Identify the blood parasite species.
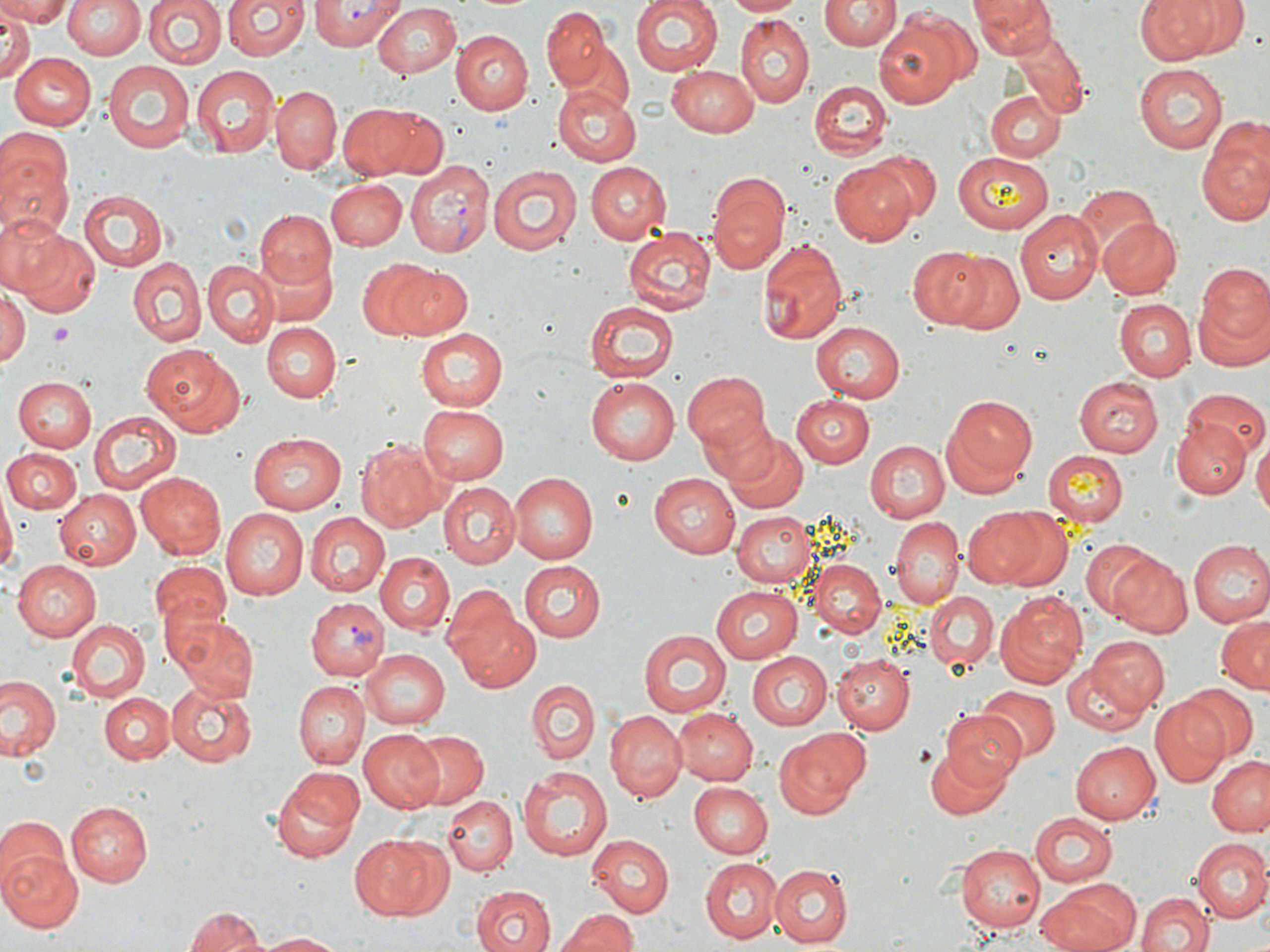
Plasmodium vivax.

Summary:
  - Coordinate format: approximate bounding boxes as named x1/y1/x2/y2 corners in pixels
  - Platelet locations: (x1=49, y1=325, x2=73, y2=345)
  - Plasmodium vivax-infected red blood cell locations: (x1=309, y1=0, x2=401, y2=50), (x1=404, y1=162, x2=493, y2=256), (x1=307, y1=599, x2=388, y2=684)
  - Uninfected red blood cell locations: (x1=1, y1=0, x2=73, y2=26), (x1=61, y1=0, x2=145, y2=60), (x1=141, y1=0, x2=225, y2=71), (x1=224, y1=0, x2=308, y2=63), (x1=629, y1=0, x2=722, y2=76), (x1=725, y1=0, x2=805, y2=17), (x1=821, y1=0, x2=897, y2=50), (x1=970, y1=0, x2=1052, y2=58), (x1=1137, y1=0, x2=1247, y2=63), (x1=369, y1=3, x2=464, y2=79), (x1=540, y1=5, x2=613, y2=92), (x1=872, y1=12, x2=971, y2=110), (x1=0, y1=14, x2=34, y2=81), (x1=734, y1=18, x2=813, y2=108), (x1=454, y1=28, x2=535, y2=113), (x1=1011, y1=31, x2=1089, y2=116), (x1=556, y1=41, x2=635, y2=115), (x1=9, y1=52, x2=96, y2=130), (x1=103, y1=60, x2=196, y2=152), (x1=1135, y1=63, x2=1227, y2=153), (x1=191, y1=65, x2=279, y2=158), (x1=666, y1=66, x2=761, y2=135), (x1=810, y1=80, x2=889, y2=160), (x1=551, y1=82, x2=643, y2=166), (x1=270, y1=85, x2=341, y2=173), (x1=985, y1=90, x2=1064, y2=163), (x1=337, y1=103, x2=420, y2=179), (x1=370, y1=107, x2=450, y2=179), (x1=1, y1=122, x2=73, y2=213), (x1=1199, y1=122, x2=1270, y2=225), (x1=869, y1=149, x2=942, y2=220), (x1=952, y1=152, x2=1053, y2=234), (x1=1, y1=160, x2=72, y2=242), (x1=584, y1=161, x2=670, y2=243), (x1=830, y1=161, x2=918, y2=244), (x1=487, y1=164, x2=581, y2=257), (x1=706, y1=173, x2=790, y2=273), (x1=327, y1=179, x2=406, y2=249), (x1=1072, y1=183, x2=1160, y2=269), (x1=79, y1=190, x2=167, y2=270), (x1=254, y1=209, x2=335, y2=291), (x1=1016, y1=210, x2=1104, y2=305), (x1=0, y1=213, x2=71, y2=293), (x1=1099, y1=217, x2=1181, y2=299), (x1=623, y1=228, x2=717, y2=315), (x1=16, y1=231, x2=100, y2=320), (x1=758, y1=238, x2=846, y2=347), (x1=908, y1=245, x2=990, y2=329), (x1=257, y1=250, x2=338, y2=327), (x1=947, y1=252, x2=1023, y2=332), (x1=357, y1=258, x2=445, y2=337), (x1=126, y1=259, x2=205, y2=344), (x1=202, y1=260, x2=278, y2=345), (x1=1194, y1=264, x2=1270, y2=361), (x1=392, y1=267, x2=473, y2=339), (x1=0, y1=289, x2=28, y2=368), (x1=584, y1=300, x2=682, y2=382), (x1=1113, y1=300, x2=1193, y2=381), (x1=809, y1=321, x2=907, y2=403), (x1=262, y1=323, x2=339, y2=402), (x1=416, y1=330, x2=509, y2=412), (x1=143, y1=343, x2=244, y2=436), (x1=681, y1=370, x2=770, y2=459), (x1=587, y1=375, x2=684, y2=464), (x1=1074, y1=376, x2=1164, y2=457), (x1=12, y1=377, x2=97, y2=453), (x1=1182, y1=389, x2=1268, y2=459), (x1=791, y1=395, x2=874, y2=467), (x1=947, y1=395, x2=1037, y2=482), (x1=417, y1=403, x2=510, y2=484), (x1=698, y1=406, x2=782, y2=491), (x1=87, y1=410, x2=181, y2=495), (x1=1173, y1=416, x2=1250, y2=499), (x1=248, y1=431, x2=347, y2=515), (x1=723, y1=433, x2=807, y2=514), (x1=355, y1=439, x2=448, y2=531), (x1=864, y1=440, x2=949, y2=524), (x1=1254, y1=440, x2=1270, y2=522), (x1=3, y1=448, x2=81, y2=515), (x1=1041, y1=450, x2=1130, y2=524), (x1=136, y1=471, x2=226, y2=559), (x1=508, y1=471, x2=597, y2=563), (x1=648, y1=472, x2=740, y2=558), (x1=439, y1=484, x2=519, y2=568), (x1=57, y1=487, x2=143, y2=571), (x1=0, y1=493, x2=15, y2=581), (x1=962, y1=506, x2=1054, y2=589), (x1=219, y1=507, x2=307, y2=600), (x1=732, y1=511, x2=818, y2=588), (x1=881, y1=512, x2=1042, y2=597), (x1=307, y1=515, x2=389, y2=597), (x1=887, y1=517, x2=964, y2=608), (x1=1080, y1=539, x2=1157, y2=620), (x1=1187, y1=539, x2=1270, y2=628), (x1=376, y1=553, x2=453, y2=633), (x1=1106, y1=553, x2=1194, y2=638), (x1=11, y1=558, x2=100, y2=640), (x1=519, y1=559, x2=606, y2=640), (x1=808, y1=559, x2=888, y2=639), (x1=149, y1=560, x2=231, y2=641), (x1=709, y1=585, x2=806, y2=661), (x1=927, y1=592, x2=998, y2=674), (x1=995, y1=593, x2=1089, y2=688), (x1=449, y1=603, x2=541, y2=691), (x1=55, y1=612, x2=221, y2=710), (x1=170, y1=613, x2=260, y2=704), (x1=1215, y1=615, x2=1270, y2=695), (x1=65, y1=619, x2=148, y2=702), (x1=638, y1=630, x2=729, y2=717), (x1=1083, y1=636, x2=1168, y2=716), (x1=360, y1=648, x2=449, y2=730), (x1=745, y1=651, x2=833, y2=730), (x1=831, y1=653, x2=913, y2=733), (x1=1060, y1=654, x2=1156, y2=737), (x1=0, y1=676, x2=62, y2=762), (x1=166, y1=679, x2=255, y2=767), (x1=528, y1=679, x2=599, y2=764), (x1=294, y1=680, x2=368, y2=768), (x1=1177, y1=684, x2=1258, y2=762), (x1=976, y1=686, x2=1058, y2=760), (x1=98, y1=691, x2=175, y2=763), (x1=1150, y1=697, x2=1230, y2=785), (x1=673, y1=709, x2=758, y2=785), (x1=939, y1=710, x2=1029, y2=794), (x1=604, y1=711, x2=685, y2=801), (x1=359, y1=728, x2=447, y2=812), (x1=772, y1=728, x2=871, y2=818), (x1=410, y1=732, x2=489, y2=806), (x1=1071, y1=741, x2=1161, y2=825), (x1=926, y1=742, x2=1012, y2=820), (x1=1207, y1=755, x2=1270, y2=838), (x1=270, y1=767, x2=363, y2=864), (x1=518, y1=767, x2=611, y2=862), (x1=690, y1=781, x2=774, y2=857), (x1=443, y1=795, x2=516, y2=875), (x1=67, y1=803, x2=153, y2=886), (x1=1029, y1=812, x2=1118, y2=885), (x1=0, y1=816, x2=69, y2=892), (x1=351, y1=832, x2=449, y2=920), (x1=586, y1=836, x2=673, y2=916), (x1=1190, y1=839, x2=1270, y2=924), (x1=957, y1=845, x2=1044, y2=933), (x1=1, y1=850, x2=83, y2=933), (x1=699, y1=855, x2=782, y2=941), (x1=770, y1=864, x2=855, y2=946), (x1=1039, y1=878, x2=1139, y2=952), (x1=472, y1=886, x2=556, y2=952), (x1=1137, y1=890, x2=1214, y2=952), (x1=184, y1=904, x2=270, y2=952), (x1=555, y1=908, x2=640, y2=952), (x1=255, y1=932, x2=345, y2=951)
  - Preparation: thin blood smear
  - Stain: May-Grünwald-Giemsa
  - Field of view: one of a larger specimen
  - Image size: 1270×952 pixels
  - Magnification: 1000x
  - Modality: light microscopy